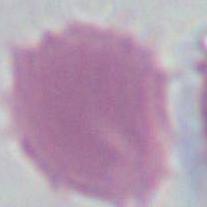

Summary:
  - Modality: photomicrograph
  - Magnification: 1000x
  - Identification: red blood cell